Locate every malaria parasite.
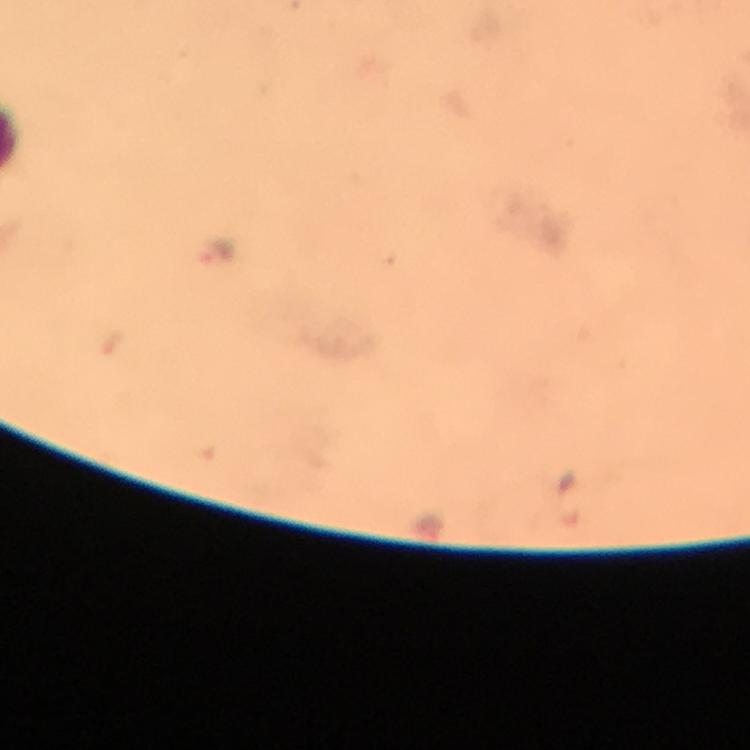
Approximate object centers, in pixels from the top-left corner.
Malaria parasites: (x=219, y=251).

Giemsa stain. At 100x magnification. Immersion oil was used. From a diagnostic examination for malaria. Thick blood film. A crop from one field of view. Image is 750×750 pixels. Photographed with a smartphone mounted on the microscope.